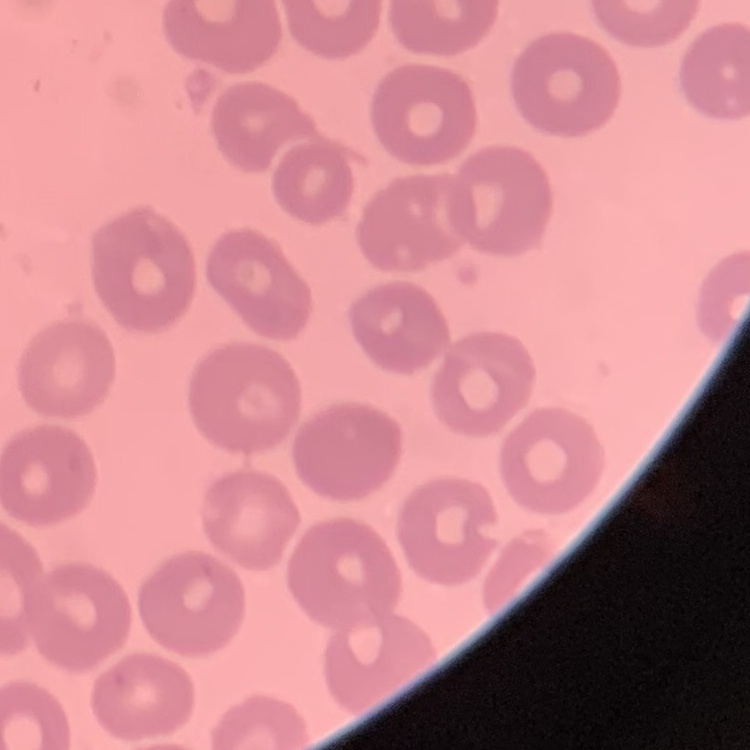

Summary:
  - Erythrocyte morphology: no rouleaux formation
  - Preparation: thin blood film
  - Stain: Field's or Giemsa
  - Image type: one tile cut from a larger photomicrograph